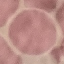
Summary:
  - Malaria status: uninfected
  - Stain: Giemsa
  - Preparation: thin blood smear
  - Capture: smartphone camera at the microscope eyepiece
  - Image type: cell patch, automatically extracted from a larger field of view and resized to 64 × 64 pixels